Report the malaria status of this cell.
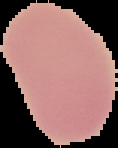
It is uninfected.

From a thin blood film. The area outside the segmented cell region is set to black. Image is 118×148 pixels.